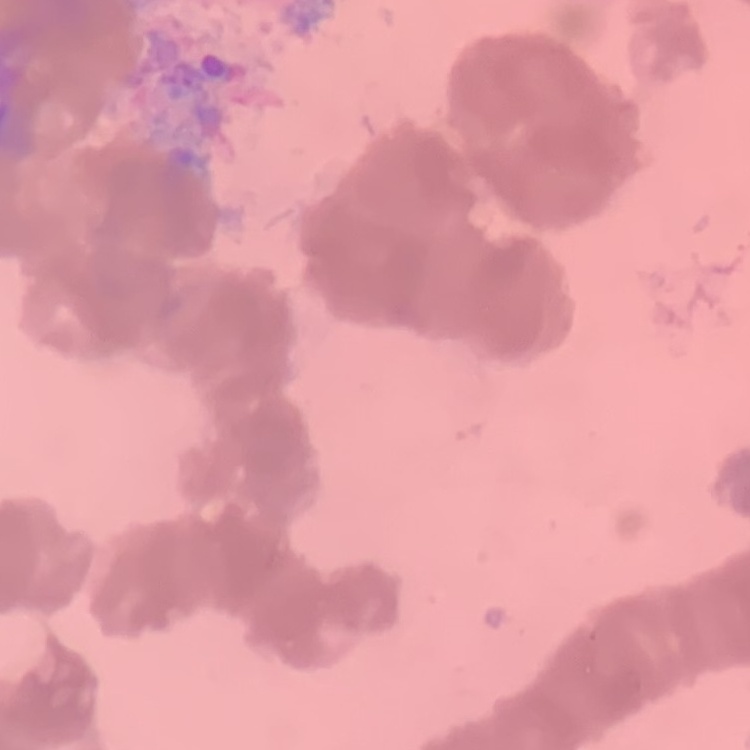
red_blood_cell_morphology: rouleaux formation
image_type: one tile cut from a larger photomicrograph
stain: Field's or Giemsa
preparation: thin peripheral smear